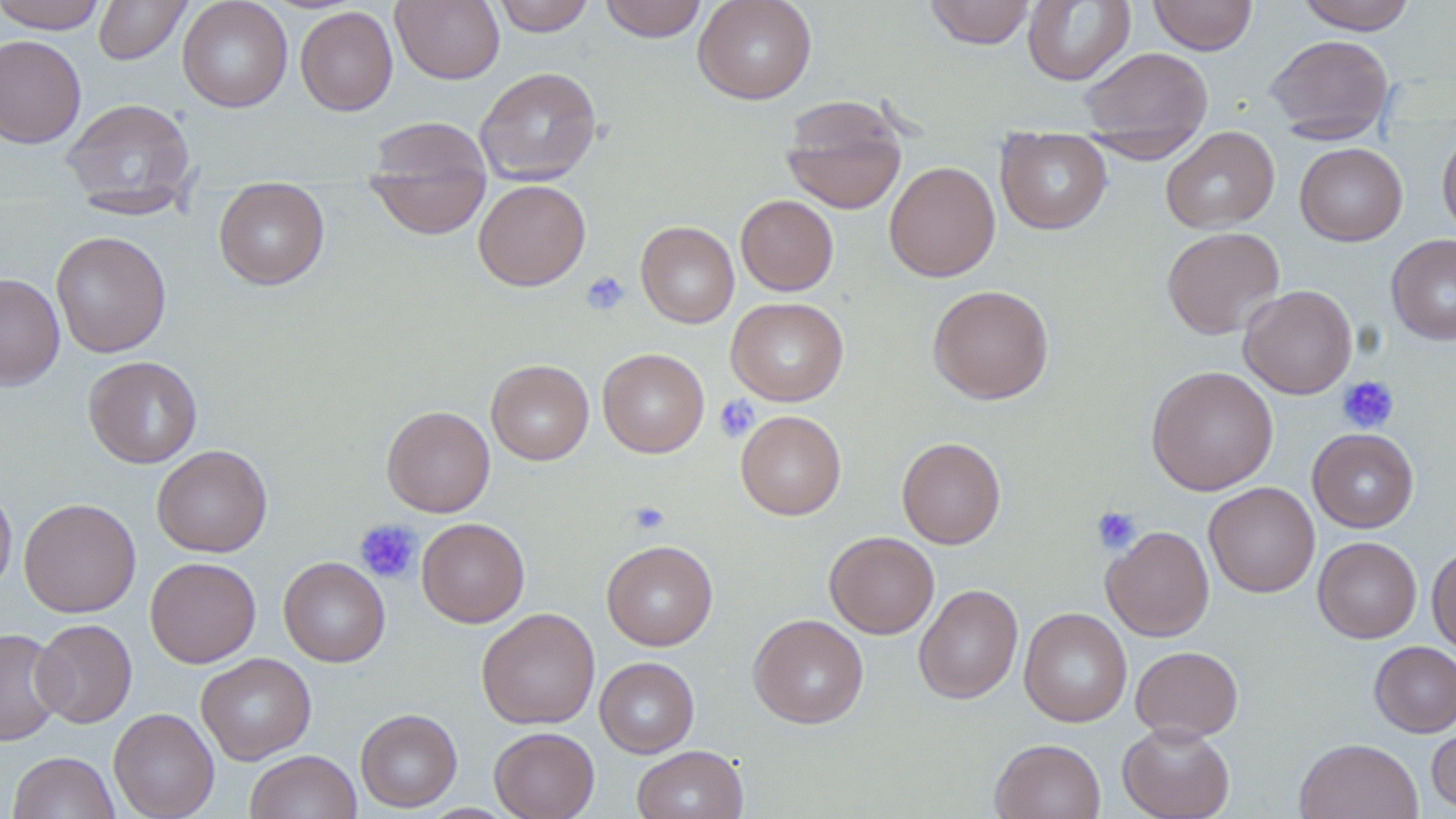 Approximate bounding boxes as [x1, y1, x2, y2] in pixels. Uninfected red blood cell locations: [0, 0, 108, 33], [93, 0, 191, 64], [177, 0, 292, 112], [391, 0, 504, 84], [490, 0, 595, 36], [598, 0, 708, 42], [692, 0, 817, 104], [924, 0, 1036, 49], [1023, 0, 1135, 86], [1149, 0, 1257, 55], [1293, 0, 1419, 33], [295, 6, 398, 115], [1265, 33, 1394, 142], [0, 34, 86, 149], [1080, 47, 1213, 148], [474, 66, 601, 185], [780, 96, 907, 215], [60, 97, 197, 214], [364, 118, 492, 234], [996, 127, 1112, 235], [1161, 127, 1279, 234], [1437, 128, 1456, 240], [1295, 142, 1407, 246], [884, 160, 1000, 282], [473, 179, 590, 291], [213, 183, 330, 290], [736, 194, 838, 296], [636, 221, 739, 328], [1161, 226, 1285, 339], [51, 230, 171, 358], [1387, 233, 1456, 345], [0, 273, 65, 391], [1239, 284, 1357, 399], [927, 285, 1054, 404], [726, 297, 849, 406], [597, 348, 709, 457], [83, 356, 202, 469], [486, 359, 594, 465], [1146, 365, 1278, 495], [381, 405, 495, 517], [735, 410, 846, 520], [1307, 428, 1419, 532], [896, 436, 1006, 549], [152, 444, 272, 557], [0, 480, 17, 595], [1204, 482, 1319, 598], [19, 498, 141, 617], [416, 517, 530, 628], [1102, 525, 1214, 642], [824, 531, 939, 638], [1313, 536, 1421, 643], [601, 540, 718, 651], [1427, 543, 1456, 654], [279, 556, 390, 667], [145, 557, 261, 668], [913, 584, 1023, 704], [476, 607, 600, 729], [1019, 607, 1132, 727], [748, 614, 869, 729], [31, 618, 137, 728], [0, 627, 66, 746], [1369, 641, 1456, 737], [1130, 645, 1243, 741], [196, 653, 316, 764], [594, 657, 700, 758], [108, 707, 219, 819], [355, 708, 462, 812], [1426, 718, 1456, 814], [1118, 722, 1235, 819], [489, 726, 600, 819], [989, 738, 1106, 819], [1294, 738, 1423, 819], [632, 745, 748, 819], [245, 750, 362, 819], [8, 751, 120, 818]. Platelet locations: [581, 270, 630, 316], [1336, 375, 1399, 433], [714, 395, 760, 443], [628, 501, 669, 534], [1091, 505, 1142, 554], [354, 519, 422, 584]. Slide-level diagnosis: negative for blood parasites. Captured at 1000x magnification. Light microscopy. Single field of view. Image is 1456×819 pixels. Thin blood smear. May-Grünwald-Giemsa-stained preparation.